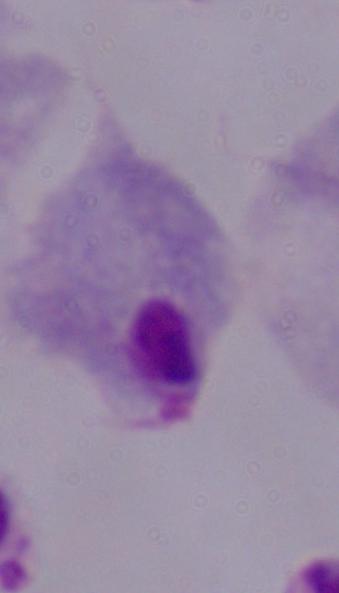
magnification = 1000x
modality = micrograph
identification = trichomonad